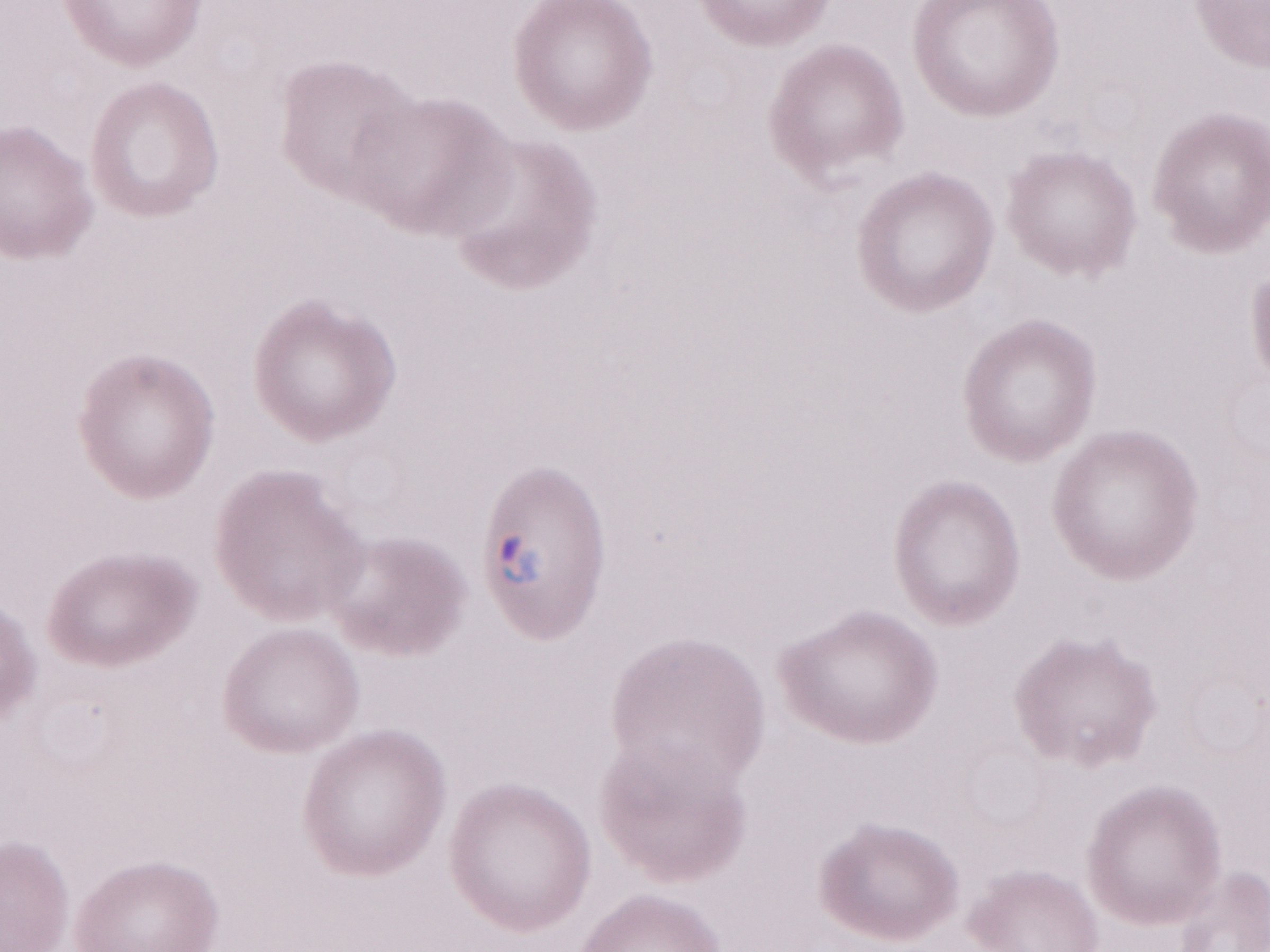 Olympus BX43 microscope, Olympus DP73 camera. Thin blood smear. Magnification: 1,000x. Patient-level malaria diagnosis: positive. Single field of view. Image is 1270×952 pixels. May-Grünwald-Giemsa stain.